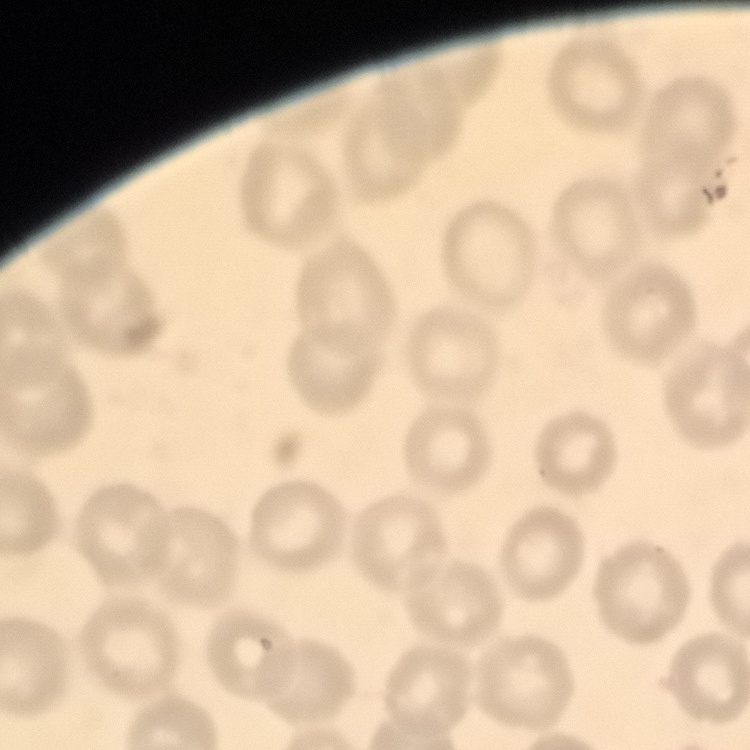
{
  "erythrocyte_morphology": "no rouleaux formation",
  "stain": "Field's or Giemsa",
  "preparation": "thin blood film",
  "image_type": "one tile cut from a larger photomicrograph"
}